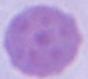
Summary:
  - Magnification: 1000x
  - Modality: micrograph
  - Identification: erythrocyte